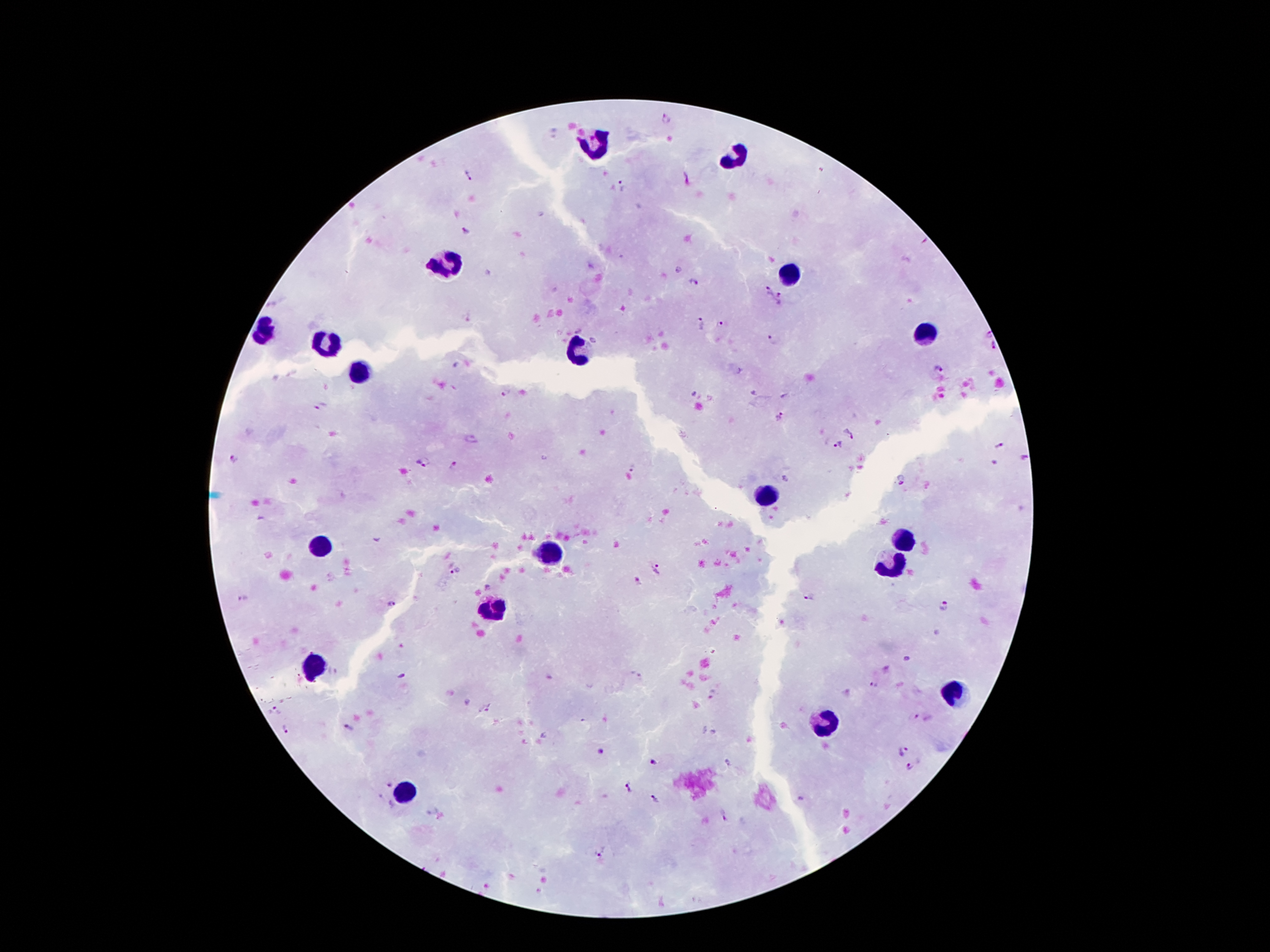
Approximate centers as {x, y} in pixels. Plasmodium parasite locations: {668, 121}, {466, 176}, {623, 187}, {466, 232}, {693, 280}, {767, 290}, {780, 299}, {700, 323}, {719, 324}, {990, 334}, {774, 339}, {992, 346}, {939, 369}, {505, 392}, {320, 406}, {779, 418}, {852, 431}, {838, 445}, {1000, 446}, {1025, 458}, {235, 459}, {424, 462}, {454, 465}, {633, 468}, {901, 480}, {455, 571}, {660, 572}, {637, 581}, {810, 598}, {243, 599}, {390, 604}, {943, 605}, {905, 659}, {402, 674}, {874, 685}, {711, 694}, {485, 710}, {274, 712}, {916, 718}, {286, 729}, {349, 730}, {903, 750}, {601, 752}, {654, 762}, {911, 767}, {389, 784}, {628, 788}, {655, 799}, {724, 816}, {601, 852}. Leukocyte locations: {596, 145}, {736, 158}, {443, 262}, {789, 270}, {266, 329}, {925, 333}, {326, 343}, {578, 351}, {360, 374}, {764, 494}, {899, 537}, {321, 550}, {550, 555}, {891, 565}, {490, 609}, {316, 667}, {952, 690}, {823, 723}, {405, 794}. Giemsa stain. Patient malaria status: infected with Plasmodium falciparum. One field from this slide. Photographed through the microscope eyepiece with a smartphone camera. 100x magnification. Thick peripheral-blood smear. Image is 1270×952 pixels.